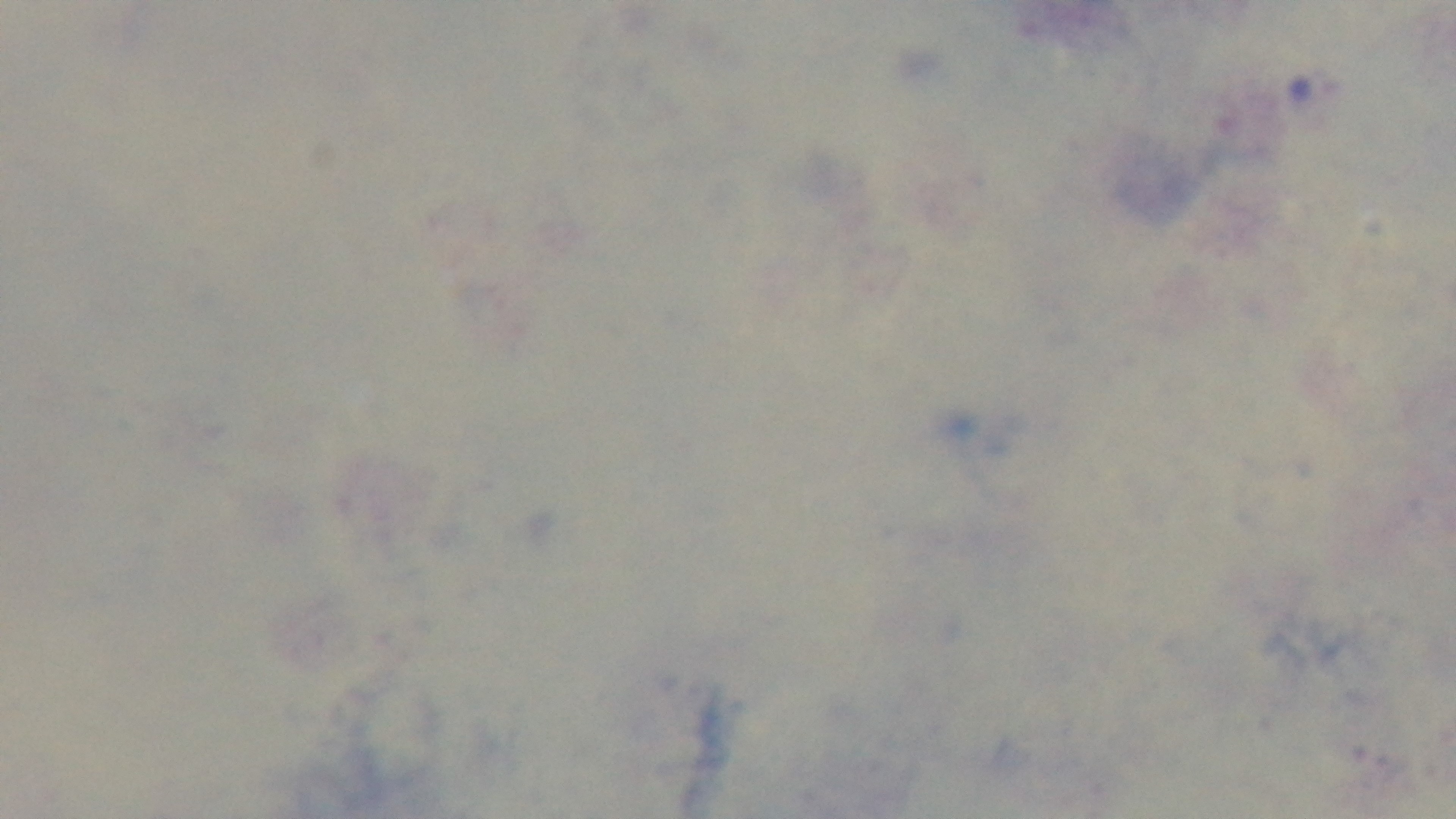
preparation = thick smear
objective = 100x oil immersion
modality = light microscopy
stain = Giemsa
capture = mounted 4K digital camera
field of view = one from the slide
malaria status = negative